Identify the cell.
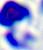
A leukocyte.

Summary:
  - Modality: photomicrograph
  - Magnification: 400x